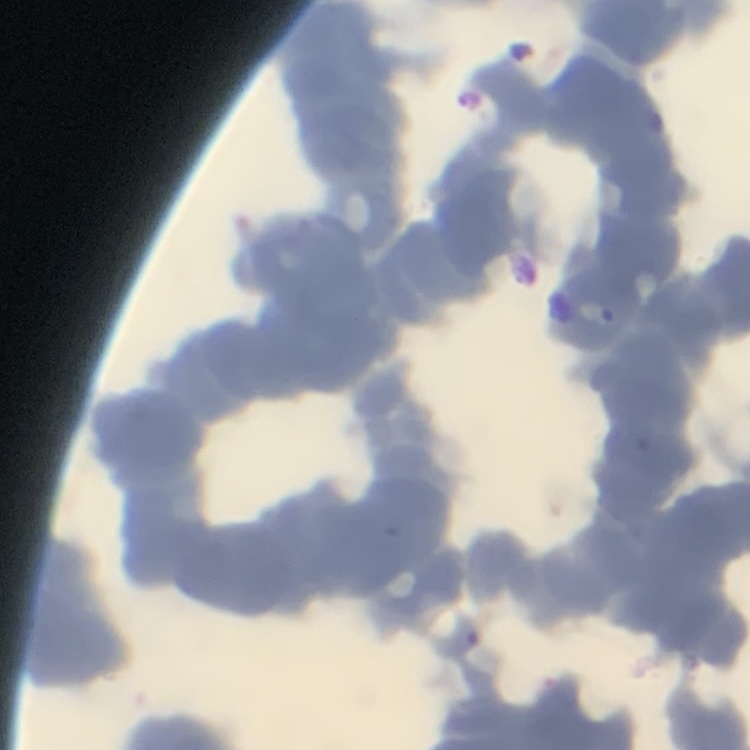

Summary:
  - Erythrocyte morphology: rouleaux formation
  - Image type: one tile cut from a larger photomicrograph
  - Stain: Field's or Giemsa
  - Preparation: thin peripheral smear